Give the extent of all Trypanosoma brucei.
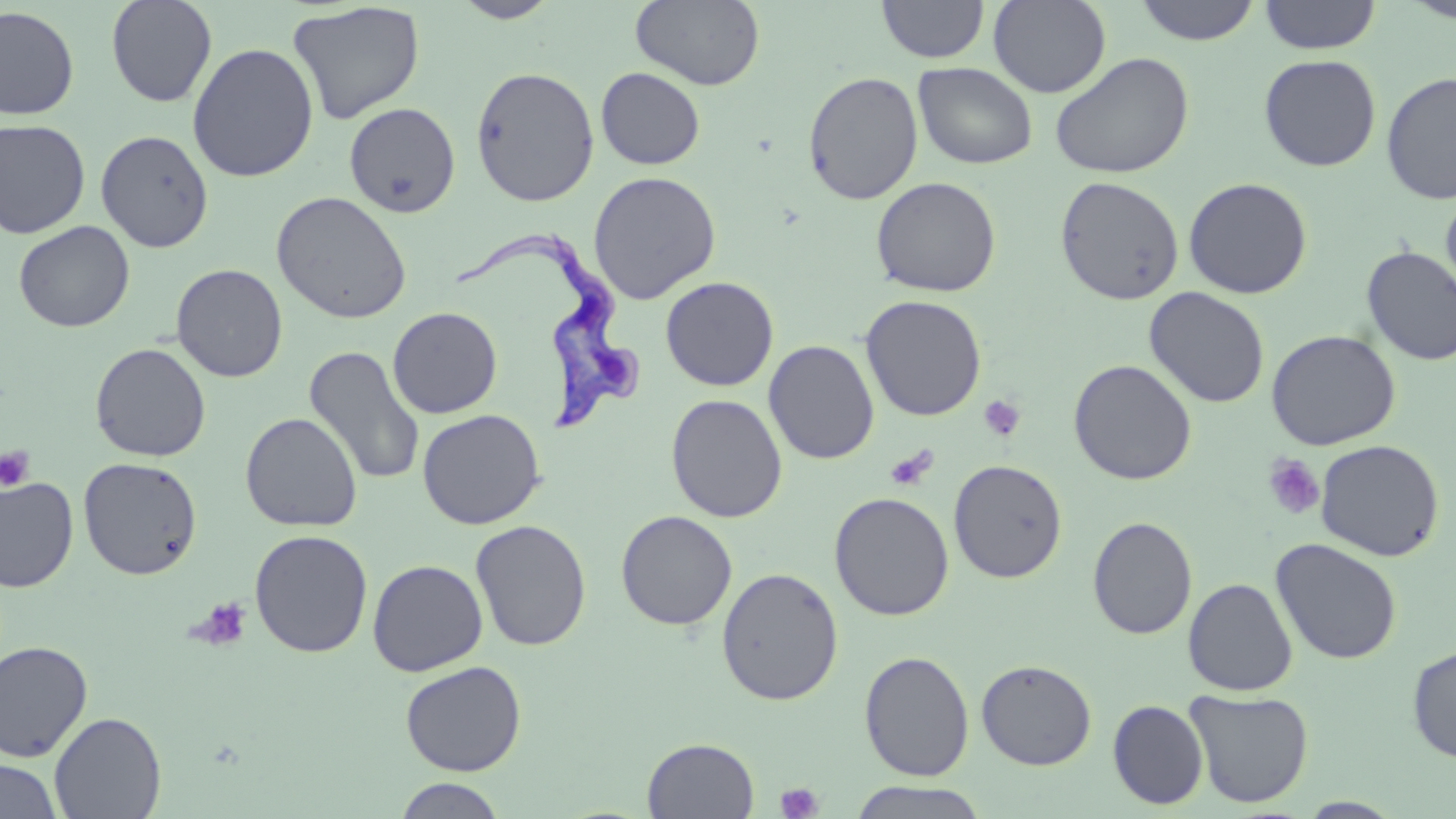

Approximate bounding boxes as (x1,y1)-(x2,y2) corner pairs in pixels.
Trypanosoma brucei: (450,229)-(645,436).

Summary:
  - Uninfected red blood cell locations: (105,0)-(218,107), (451,0)-(562,23), (630,0)-(766,91), (988,0)-(1111,97), (1132,0)-(1262,45), (1258,0)-(1382,55), (1400,0)-(1456,24), (288,1)-(425,125), (877,1)-(989,63), (0,6)-(79,120), (187,43)-(319,182), (1050,52)-(1194,179), (1259,54)-(1382,171), (913,63)-(1038,169), (470,66)-(599,207), (596,67)-(705,170), (803,71)-(924,205), (1381,71)-(1456,205), (344,101)-(461,219), (0,119)-(91,239), (95,129)-(214,253), (587,170)-(722,304), (1054,175)-(1185,306), (871,176)-(1001,297), (1183,177)-(1312,299), (1440,188)-(1456,311), (271,191)-(412,324), (13,220)-(135,333), (1360,246)-(1456,366), (171,263)-(288,382), (660,276)-(779,391), (1144,287)-(1271,408), (860,295)-(987,421), (387,306)-(503,418), (1266,329)-(1401,451), (764,340)-(880,465), (90,342)-(211,462), (304,345)-(425,487), (1068,359)-(1197,486), (666,394)-(788,523), (417,408)-(546,529), (240,412)-(363,532), (1315,439)-(1445,561), (78,457)-(203,579), (948,459)-(1068,583), (0,476)-(78,592), (829,492)-(954,620), (616,509)-(738,630), (1087,516)-(1198,640), (471,519)-(592,652), (249,529)-(373,658), (1270,538)-(1402,665), (367,559)-(488,676), (716,567)-(844,706), (1183,578)-(1299,696), (0,641)-(93,762), (1407,645)-(1456,763), (859,650)-(975,781), (976,659)-(1097,770), (400,660)-(527,776), (1185,688)-(1314,808), (1107,700)-(1209,810), (49,711)-(167,819), (642,737)-(760,819), (0,758)-(64,819), (391,777)-(509,818), (847,781)-(989,818), (1296,797)-(1407,818)
  - Platelet locations: (978,395)-(1026,442), (0,446)-(35,492), (884,446)-(938,491), (1262,454)-(1326,520), (188,597)-(252,651), (775,782)-(824,819)
  - Slide-level diagnosis: Trypanosoma brucei
  - Preparation: thin blood smear
  - Stain: May-Grünwald-Giemsa
  - Field of view: single
  - Image size: 1456×819 pixels
  - Modality: optical microscopy
  - Magnification: 1000x